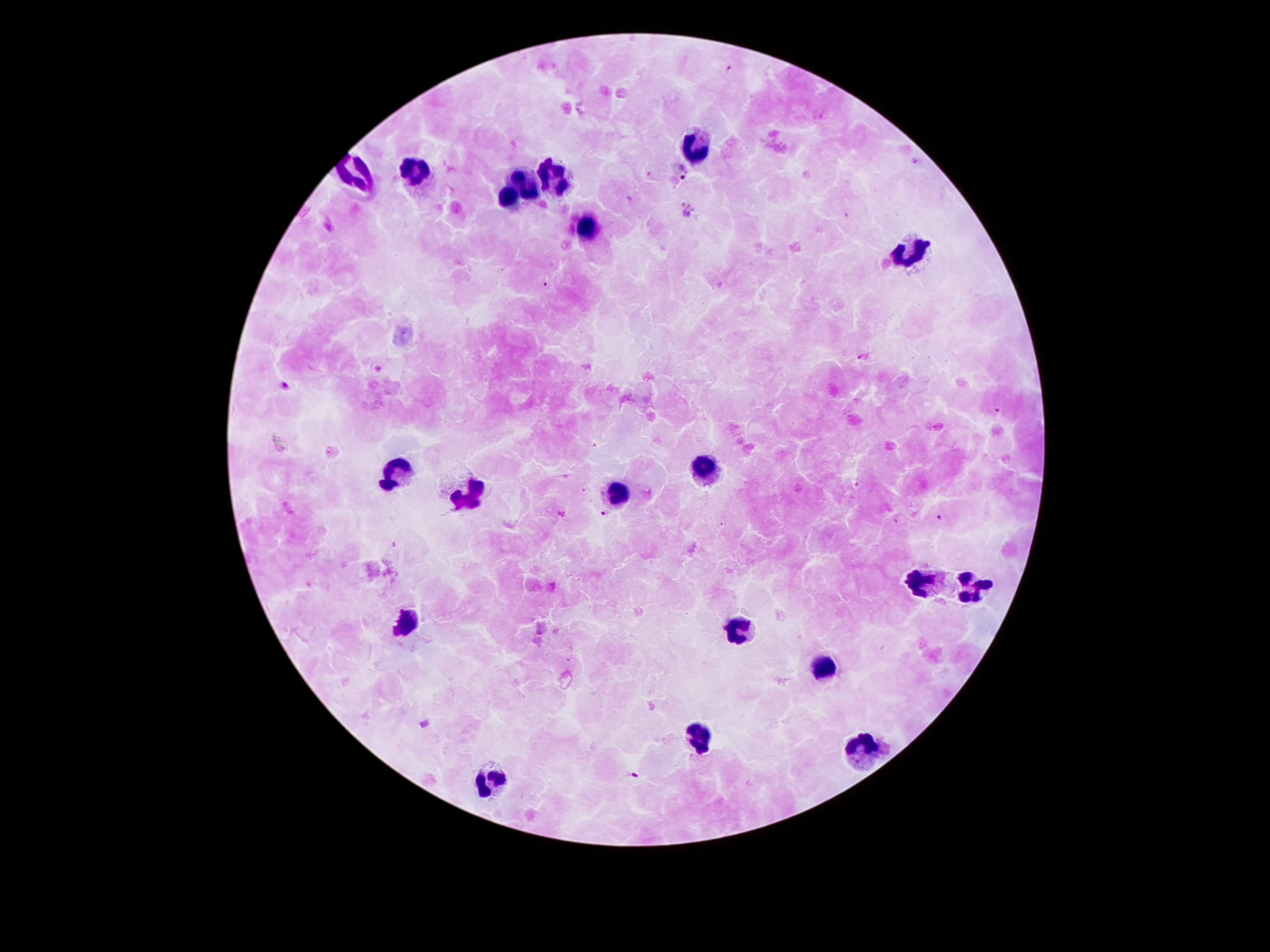
Approximate centers as [x, y] in pixels.
Summary:
  - Malaria parasite locations: [730, 67], [546, 285], [860, 356], [287, 386], [996, 410], [606, 514], [939, 517], [636, 775]
  - Leukocyte locations: [694, 145], [418, 171], [526, 183], [554, 183], [510, 200], [588, 226], [912, 250], [704, 466], [394, 472], [612, 492], [466, 494], [964, 582], [922, 584], [404, 620], [738, 630], [824, 667], [698, 737], [864, 751], [486, 777]
  - Magnification: 100x
  - Patient malaria status: infected with Plasmodium falciparum
  - Field of view: single
  - Preparation: thick blood film
  - Capture: smartphone through the microscope eyepiece
  - Image size: 1270×952 pixels
  - Stain: Giemsa